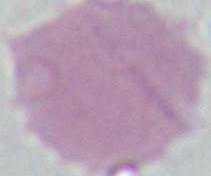
Micrograph. Captured at 1000x magnification. A red blood cell is seen.